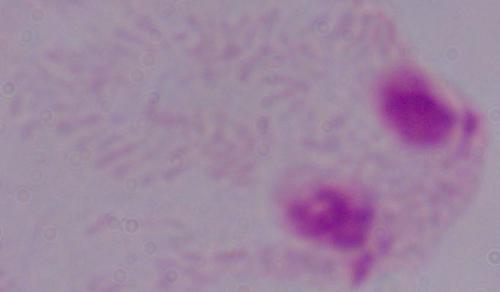 1000x magnification. A trichomonad is seen. Micrograph.